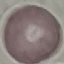

result = no malaria parasites detected
preparation = thin blood smear
image type = cell patch, automatically extracted from a larger field of view and resized to 64 × 64 pixels
stain = Giemsa
capture = smartphone camera at the microscope eyepiece